Classify this cell by malaria status.
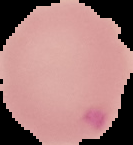
It is parasitized.

The area outside the segmented cell region is set to black. From a thin blood smear. Image is 133×145 pixels.